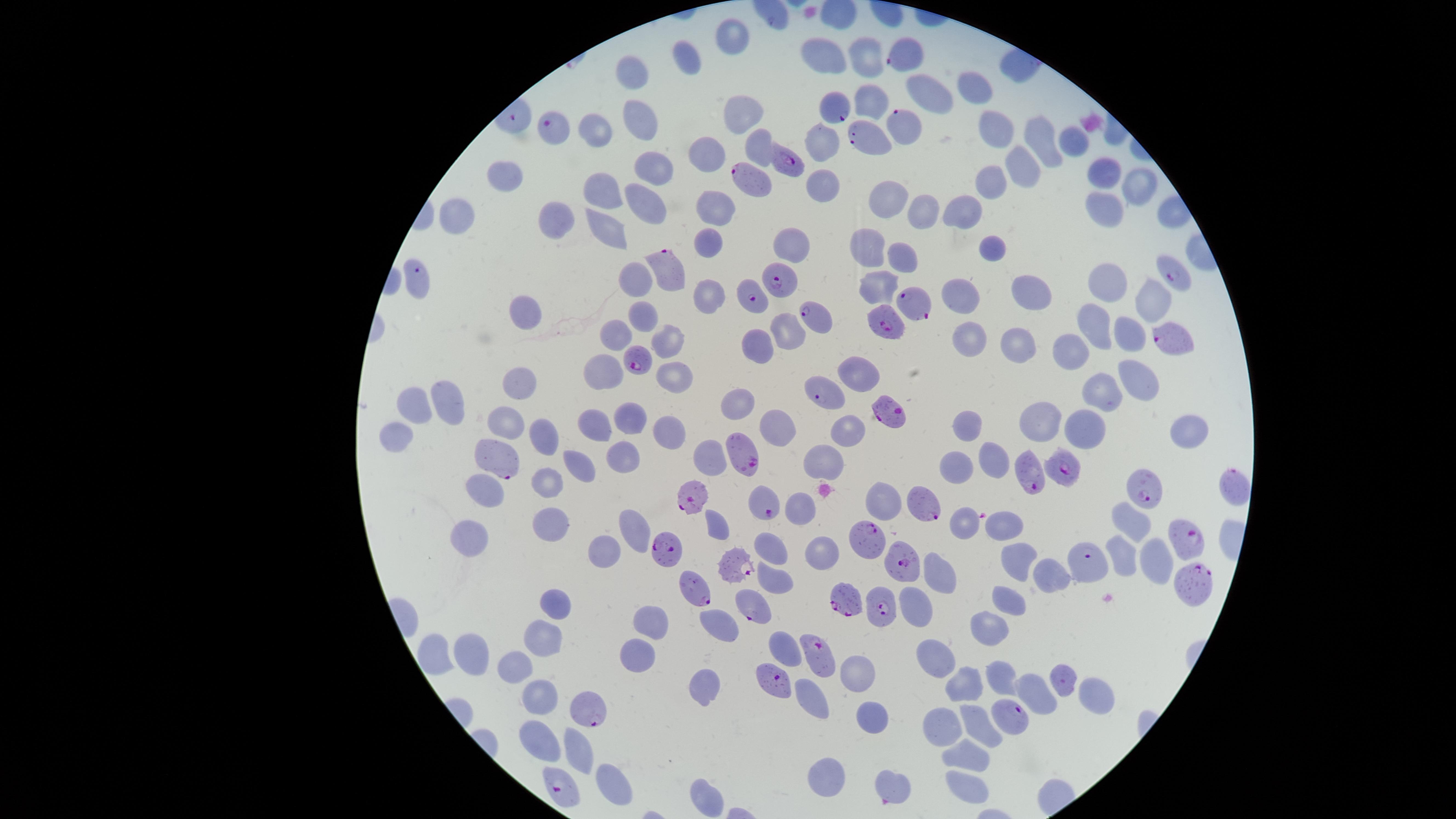 Approximate marker points as {x, y} in pixels. Parasitized red blood cells: {909, 55}, {836, 111}, {556, 122}, {903, 126}, {864, 136}, {790, 160}, {752, 180}, {664, 271}, {1176, 273}, {420, 282}, {784, 283}, {752, 295}, {914, 300}, {810, 319}, {884, 323}, {1169, 340}, {639, 360}, {822, 391}, {888, 413}, {745, 450}, {494, 454}, {1061, 467}, {1028, 475}, {1230, 490}, {1144, 491}, {692, 496}, {766, 503}, {926, 505}, {867, 536}, {1191, 542}, {668, 547}, {905, 562}, {1082, 564}, {732, 568}, {698, 587}, {1194, 587}, {845, 601}, {879, 603}, {755, 616}, {815, 653}, {772, 680}, {590, 711}, {1010, 714}, {562, 789}. Uninfected red blood cells: {735, 32}, {865, 56}, {685, 59}, {830, 59}, {631, 73}, {979, 85}, {923, 91}, {873, 102}, {741, 117}, {639, 122}, {593, 127}, {996, 129}, {1044, 138}, {824, 143}, {1073, 145}, {757, 148}, {709, 152}, {1020, 165}, {657, 168}, {1100, 171}, {510, 176}, {992, 176}, {822, 184}, {1140, 186}, {607, 190}, {888, 197}, {640, 200}, {721, 204}, {1109, 207}, {960, 210}, {920, 211}, {456, 213}, {552, 215}, {609, 230}, {790, 243}, {708, 244}, {869, 246}, {992, 246}, {903, 255}, {635, 273}, {882, 283}, {1100, 285}, {1032, 290}, {964, 294}, {715, 297}, {1149, 300}, {525, 308}, {644, 318}, {1095, 321}, {794, 329}, {1125, 333}, {615, 335}, {963, 338}, {1016, 341}, {752, 342}, {670, 347}, {1068, 347}, {858, 370}, {606, 371}, {672, 379}, {520, 380}, {1139, 383}, {1105, 390}, {449, 401}, {420, 402}, {742, 405}, {1032, 414}, {630, 417}, {777, 419}, {1072, 421}, {593, 422}, {966, 422}, {503, 424}, {1179, 431}, {849, 433}, {665, 436}, {399, 437}, {543, 437}, {619, 455}, {710, 457}, {990, 457}, {821, 460}, {581, 466}, {953, 469}, {546, 480}, {481, 489}, {884, 501}, {801, 512}, {964, 520}, {1127, 520}, {1005, 521}, {717, 525}, {638, 527}, {543, 529}, {469, 544}, {775, 549}, {597, 552}, {1015, 553}, {820, 555}, {1152, 556}, {1120, 557}, {938, 573}, {1046, 574}, {778, 578}, {559, 602}, {1005, 602}, {916, 607}, {647, 617}, {715, 623}, {990, 626}, {541, 646}, {783, 650}, {437, 655}, {471, 655}, {937, 655}, {639, 657}, {520, 665}, {862, 675}, {1002, 676}, {1060, 676}, {959, 684}, {703, 688}, {1034, 689}, {1094, 690}, {540, 697}, {822, 704}, {869, 717}, {978, 718}, {942, 727}, {539, 740}, {576, 749}, {965, 753}, {828, 772}, {894, 781}, {607, 783}, {963, 783}, {704, 797}. Image is 1456×819 pixels. One field of view of the specimen. Circular visible region. Species: Plasmodium falciparum. Giemsa-stained preparation. Presence: malaria parasites seen. Photographed with a smartphone camera through the microscope eyepiece. Thin blood film.